Locate and identify every blood parasite.
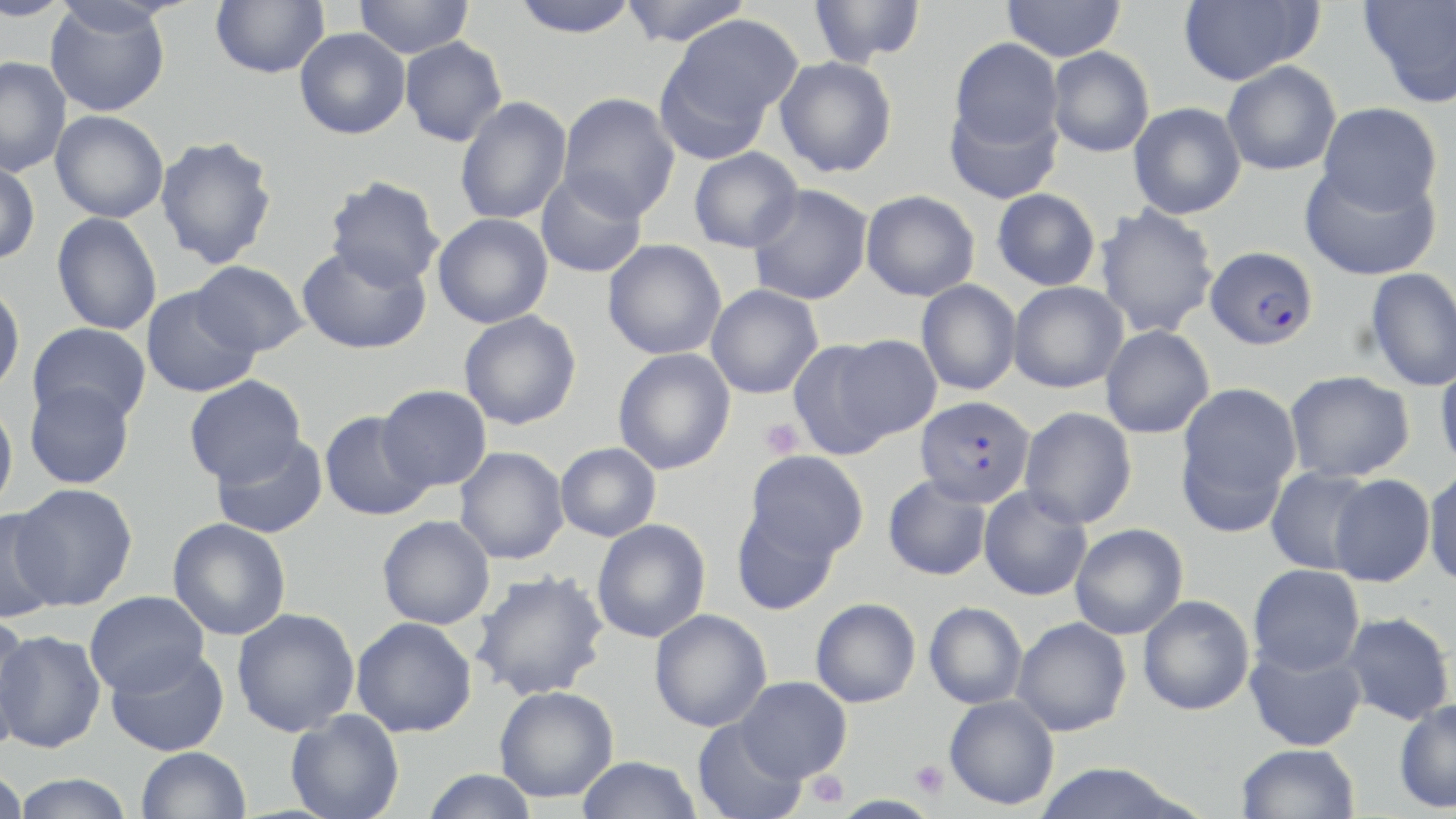
Approximate bounding boxes as named x1/y1/x2/y2 corners in pixels.
Plasmodium falciparum-infected red blood cells: (x1=1204, y1=245, x2=1319, y2=350), (x1=914, y1=396, x2=1035, y2=507).
No Plasmodium ovale, Plasmodium malariae, Plasmodium vivax, Babesia divergens, or Trypanosoma brucei observed.

Platelet locations: (x1=759, y1=419, x2=803, y2=459), (x1=910, y1=760, x2=949, y2=798), (x1=807, y1=770, x2=848, y2=809). Uninfected red blood cell locations: (x1=0, y1=0, x2=72, y2=22), (x1=210, y1=0, x2=329, y2=78), (x1=354, y1=0, x2=474, y2=59), (x1=509, y1=0, x2=642, y2=39), (x1=618, y1=0, x2=753, y2=47), (x1=809, y1=0, x2=926, y2=68), (x1=1001, y1=0, x2=1126, y2=62), (x1=1177, y1=0, x2=1323, y2=86), (x1=1359, y1=0, x2=1456, y2=109), (x1=44, y1=2, x2=172, y2=117), (x1=657, y1=14, x2=801, y2=154), (x1=294, y1=28, x2=410, y2=140), (x1=400, y1=36, x2=507, y2=147), (x1=948, y1=38, x2=1063, y2=156), (x1=1047, y1=46, x2=1155, y2=158), (x1=0, y1=56, x2=72, y2=176), (x1=774, y1=56, x2=898, y2=178), (x1=1221, y1=61, x2=1341, y2=176), (x1=558, y1=92, x2=680, y2=221), (x1=945, y1=95, x2=1063, y2=206), (x1=455, y1=96, x2=572, y2=226), (x1=1128, y1=102, x2=1246, y2=219), (x1=1316, y1=103, x2=1443, y2=216), (x1=50, y1=110, x2=169, y2=223), (x1=155, y1=135, x2=278, y2=269), (x1=688, y1=147, x2=803, y2=253), (x1=0, y1=160, x2=41, y2=265), (x1=1299, y1=162, x2=1442, y2=282), (x1=535, y1=170, x2=648, y2=278), (x1=324, y1=175, x2=445, y2=290), (x1=747, y1=184, x2=873, y2=305), (x1=991, y1=188, x2=1101, y2=291), (x1=860, y1=190, x2=980, y2=301), (x1=1094, y1=204, x2=1220, y2=339), (x1=51, y1=212, x2=162, y2=336), (x1=433, y1=213, x2=553, y2=328), (x1=602, y1=239, x2=727, y2=360), (x1=295, y1=243, x2=431, y2=355), (x1=190, y1=259, x2=310, y2=357), (x1=1365, y1=268, x2=1456, y2=392), (x1=916, y1=280, x2=1022, y2=395), (x1=1008, y1=281, x2=1128, y2=393), (x1=0, y1=282, x2=25, y2=396), (x1=705, y1=285, x2=824, y2=399), (x1=141, y1=286, x2=261, y2=398), (x1=458, y1=310, x2=582, y2=430), (x1=27, y1=322, x2=152, y2=426), (x1=1100, y1=326, x2=1215, y2=439), (x1=797, y1=334, x2=938, y2=453), (x1=613, y1=348, x2=736, y2=475), (x1=1435, y1=361, x2=1456, y2=473), (x1=1284, y1=370, x2=1415, y2=482), (x1=183, y1=375, x2=307, y2=485), (x1=24, y1=380, x2=136, y2=490), (x1=1175, y1=382, x2=1301, y2=529), (x1=377, y1=384, x2=493, y2=492), (x1=0, y1=400, x2=19, y2=513), (x1=1019, y1=407, x2=1137, y2=528), (x1=320, y1=411, x2=434, y2=522), (x1=210, y1=432, x2=328, y2=539), (x1=555, y1=442, x2=661, y2=542), (x1=454, y1=447, x2=569, y2=565), (x1=745, y1=450, x2=868, y2=560), (x1=1423, y1=466, x2=1456, y2=589), (x1=1265, y1=467, x2=1375, y2=575), (x1=1328, y1=474, x2=1435, y2=587), (x1=882, y1=475, x2=992, y2=581), (x1=10, y1=484, x2=137, y2=610), (x1=979, y1=485, x2=1093, y2=601), (x1=730, y1=505, x2=842, y2=615), (x1=0, y1=508, x2=65, y2=623), (x1=377, y1=515, x2=495, y2=630), (x1=167, y1=518, x2=292, y2=641), (x1=591, y1=519, x2=711, y2=643), (x1=1070, y1=523, x2=1188, y2=639), (x1=1248, y1=564, x2=1365, y2=676), (x1=469, y1=570, x2=609, y2=701), (x1=84, y1=590, x2=210, y2=696), (x1=1138, y1=595, x2=1254, y2=715), (x1=810, y1=598, x2=921, y2=708), (x1=924, y1=601, x2=1028, y2=710), (x1=232, y1=608, x2=360, y2=737), (x1=649, y1=609, x2=772, y2=732), (x1=1340, y1=611, x2=1454, y2=725), (x1=351, y1=617, x2=477, y2=737), (x1=1012, y1=617, x2=1131, y2=736), (x1=0, y1=622, x2=44, y2=756), (x1=0, y1=630, x2=106, y2=753), (x1=1244, y1=639, x2=1367, y2=752), (x1=105, y1=646, x2=229, y2=756), (x1=735, y1=676, x2=851, y2=782), (x1=493, y1=685, x2=619, y2=802), (x1=944, y1=695, x2=1059, y2=810), (x1=1393, y1=699, x2=1456, y2=814), (x1=285, y1=710, x2=404, y2=819), (x1=692, y1=719, x2=809, y2=819), (x1=1236, y1=743, x2=1361, y2=819), (x1=135, y1=747, x2=251, y2=819), (x1=575, y1=756, x2=703, y2=818), (x1=1033, y1=763, x2=1193, y2=819), (x1=420, y1=768, x2=540, y2=819), (x1=0, y1=769, x2=29, y2=818), (x1=10, y1=773, x2=136, y2=819). Slide-level diagnosis: Plasmodium falciparum. Single field of view. Image is 1456×819 pixels. May-Grünwald-Giemsa-stained preparation. Captured at 1000x magnification. Thin blood film. Optical microscopy.